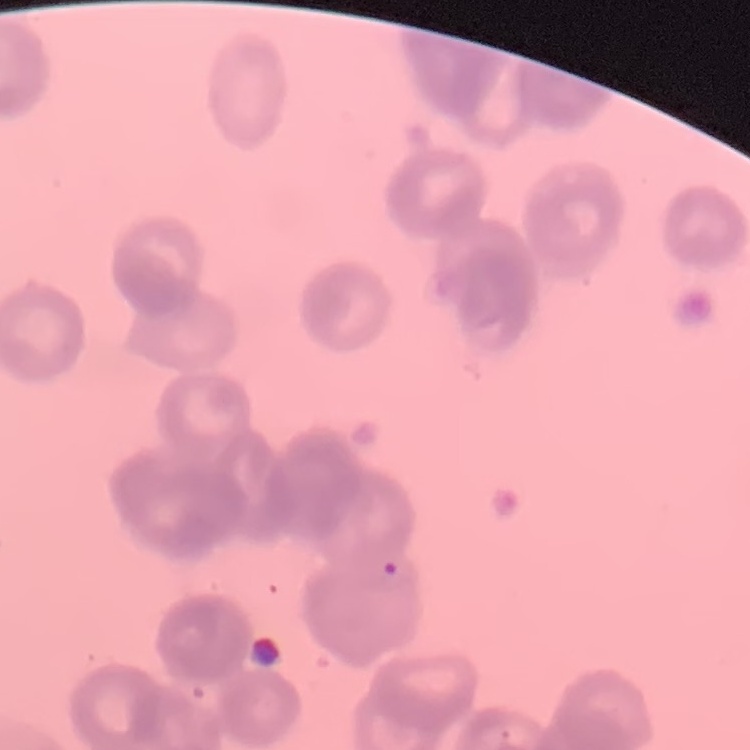

Summary:
  - Red blood cell morphology: rouleaux formation
  - Image type: one tile cut from a larger photomicrograph
  - Stain: Field's or Giemsa
  - Preparation: thin blood smear